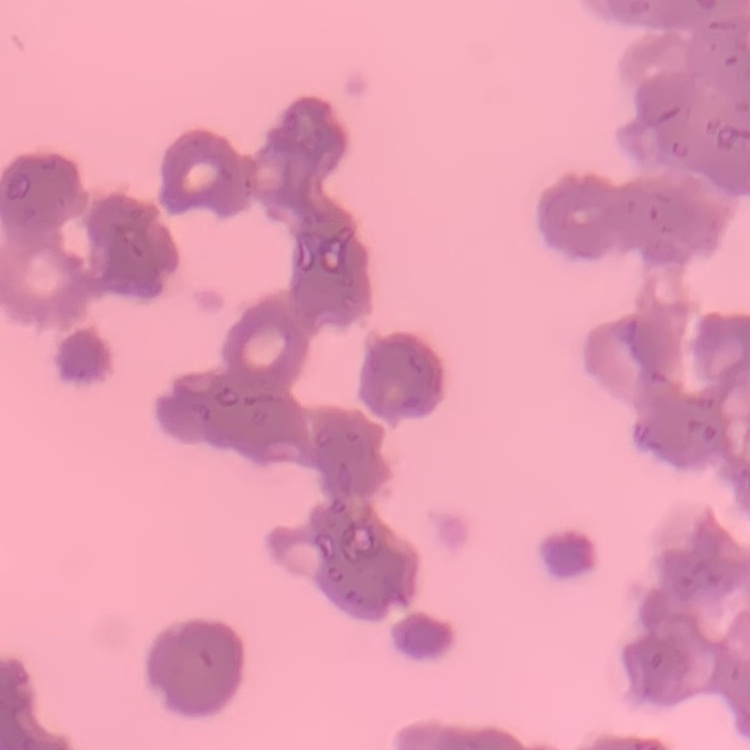
erythrocyte morphology = rouleaux formation
stain = Field's or Giemsa
image type = one tile cut from a larger photomicrograph
preparation = thin peripheral smear